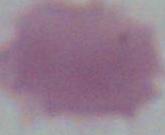
An erythrocyte is seen. Micrograph. 1000x magnification.